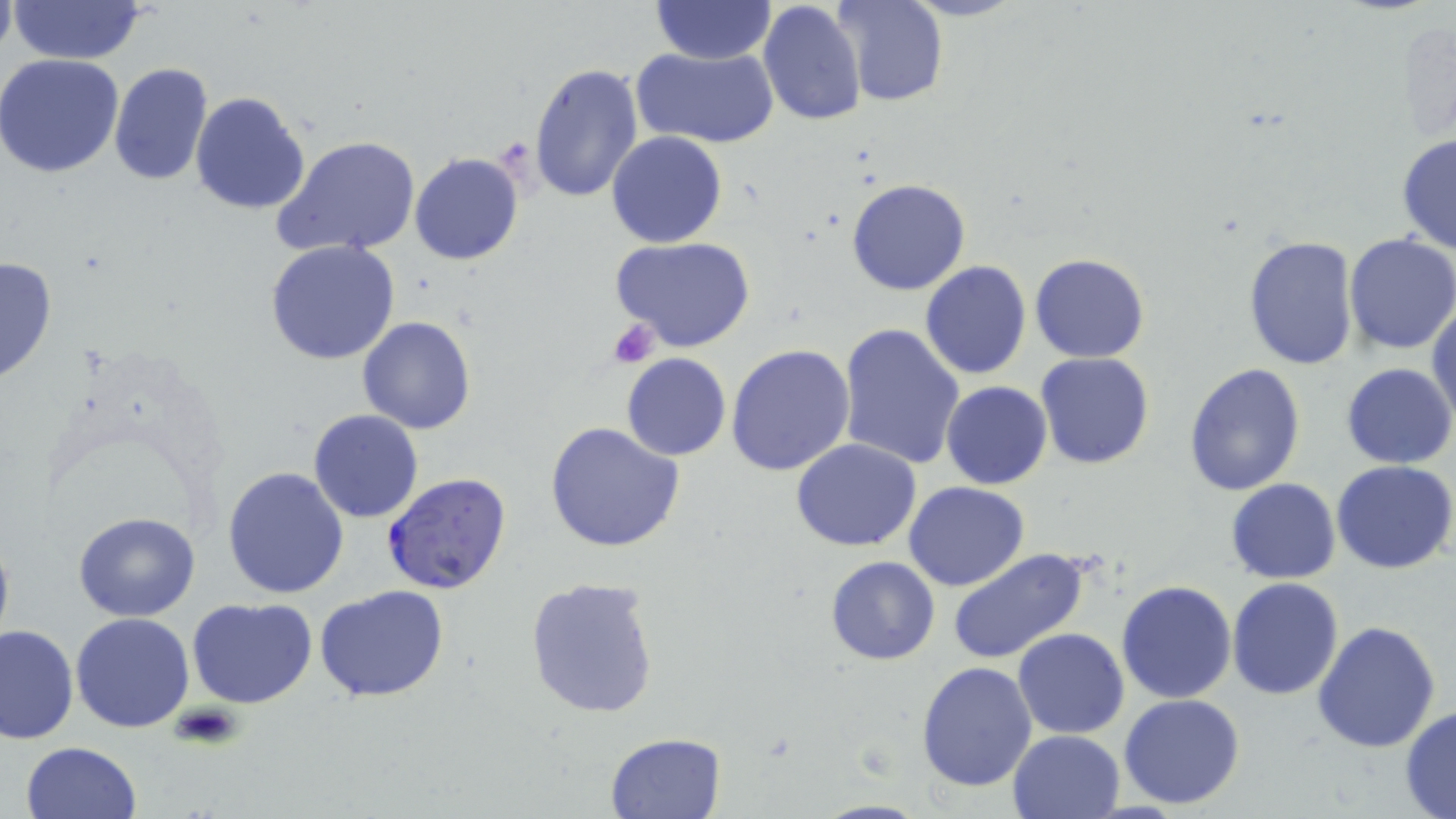

slide-level diagnosis = Plasmodium falciparum
platelet locations = approximate bounding boxes as (x1, y1, x2, y2) in pixels: (607, 319, 662, 368), (173, 700, 244, 751)
modality = optical microscopy
field of view = single
preparation = thin blood smear
magnification = 1000x
Plasmodium falciparum-infected red blood cell locations = approximate bounding boxes as (x1, y1, x2, y2) in pixels: (382, 471, 513, 594)
uninfected red blood cell locations = approximate bounding boxes as (x1, y1, x2, y2) in pixels: (8, 0, 150, 63), (651, 0, 775, 65), (835, 0, 948, 106), (757, 1, 866, 124), (632, 45, 779, 150), (0, 54, 124, 177), (528, 61, 645, 204), (107, 63, 212, 184), (190, 91, 311, 214), (606, 130, 728, 248), (1396, 133, 1456, 254), (272, 135, 421, 260), (409, 152, 524, 266), (845, 179, 971, 296), (1343, 234, 1456, 356), (1242, 235, 1360, 371), (610, 237, 755, 354), (264, 240, 400, 366), (1029, 253, 1149, 362), (0, 255, 58, 385), (920, 261, 1032, 381), (1428, 300, 1456, 428), (358, 316, 476, 434), (838, 323, 967, 470), (726, 344, 855, 477), (1036, 353, 1153, 470), (620, 354, 731, 462), (1341, 363, 1454, 468), (1185, 364, 1305, 499), (941, 381, 1052, 489), (307, 409, 424, 523), (544, 420, 686, 555), (792, 438, 923, 551), (1331, 460, 1456, 573), (222, 465, 350, 598), (1226, 479, 1342, 583), (904, 481, 1029, 592), (73, 512, 200, 622), (0, 532, 15, 654), (948, 547, 1090, 665), (826, 556, 940, 665), (524, 577, 662, 722), (1227, 577, 1344, 700), (1116, 580, 1236, 703), (315, 583, 450, 704), (187, 597, 317, 708), (70, 612, 196, 732), (1313, 622, 1442, 753), (0, 624, 79, 745), (1013, 627, 1129, 740), (917, 661, 1038, 793), (1118, 693, 1247, 809), (1400, 706, 1456, 817), (1007, 730, 1127, 819), (605, 732, 726, 819), (19, 740, 144, 819), (811, 799, 930, 818)
image size = 1456×819 pixels
stain = May-Grünwald-Giemsa